Give the position of every malaria parasite.
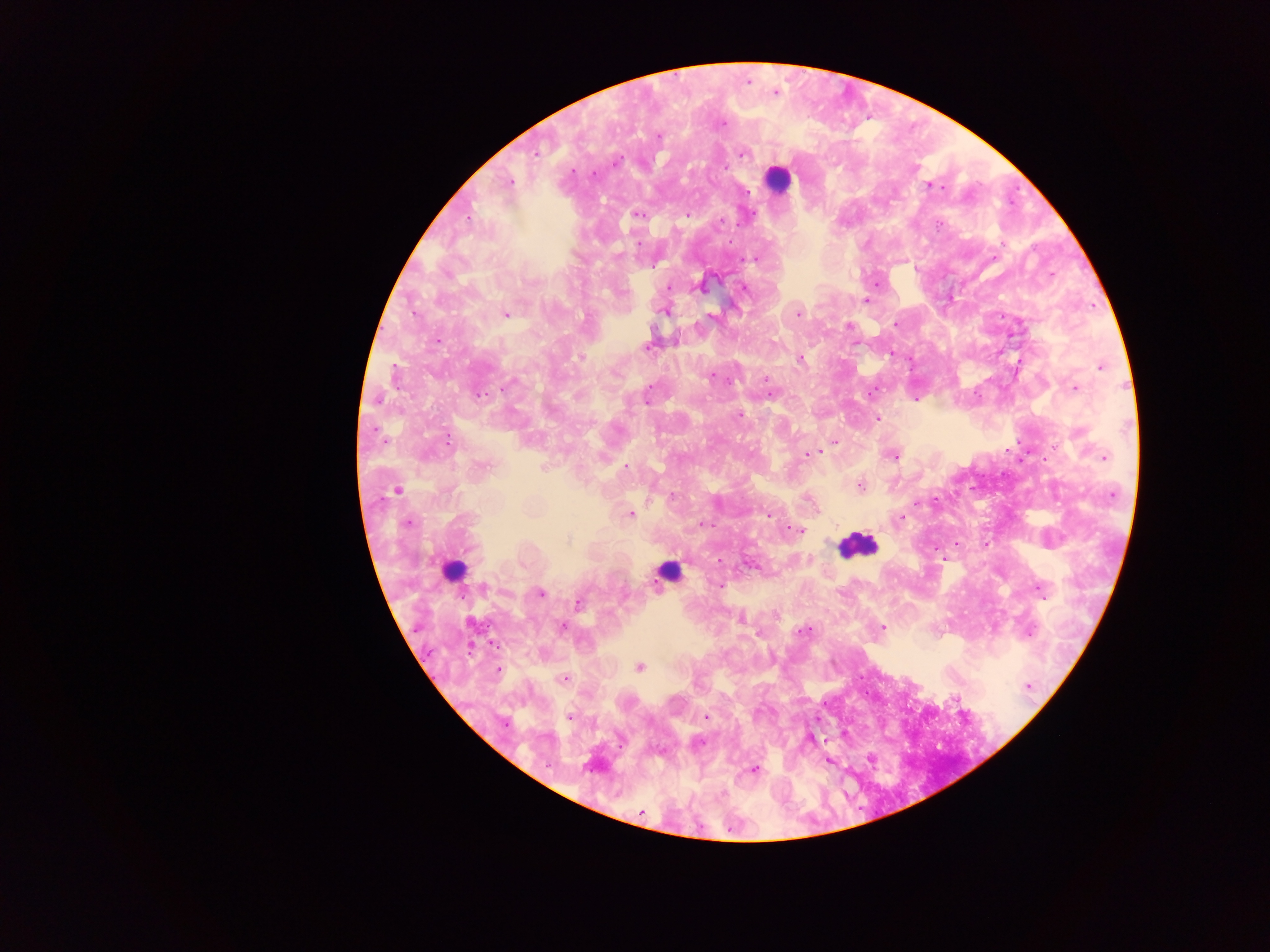

Approximate centers as x y in pixels.
Malaria parasites: 776 93; 723 125; 658 136; 536 152; 744 154; 617 162; 726 167; 593 173; 509 182; 929 186; 747 191; 637 215; 687 215; 750 215; 468 219; 721 221; 639 243; 754 259; 669 286; 702 287; 745 288; 866 301; 664 312; 506 314; 798 314; 711 316; 895 324; 849 327; 438 340; 646 348; 581 357; 800 359; 1101 366; 712 376; 766 380; 510 384; 649 387; 1075 388; 871 392; 480 394; 772 394; 915 398; 377 399; 645 401; 739 415; 877 418; 447 440; 834 441; 815 453; 808 454; 893 457; 1103 457; 484 466; 543 467; 625 467; 860 485; 396 491; 672 496; 917 503; 630 514; 767 515; 901 518; 407 523; 705 524; 797 530; 568 540; 957 543; 753 565; 719 586; 1040 589; 540 594; 578 605; 740 619; 563 627; 882 627; 803 631; 639 667; 499 669; 565 679; 1029 686; 569 717; 706 717; 700 743; 754 769; 641 812.
Each of these objects is labeled both malaria parasite and leukocyte by the source: 452 569; 667 571.

Summary:
  - Leukocyte locations (subset; some below the resolvable size): 777 178; 857 546
  - Country: Ghana
  - Field of view: single
  - Capture: mobile-phone photograph through a microscope
  - Image size: 1270×952 pixels
  - Preparation: thick blood film